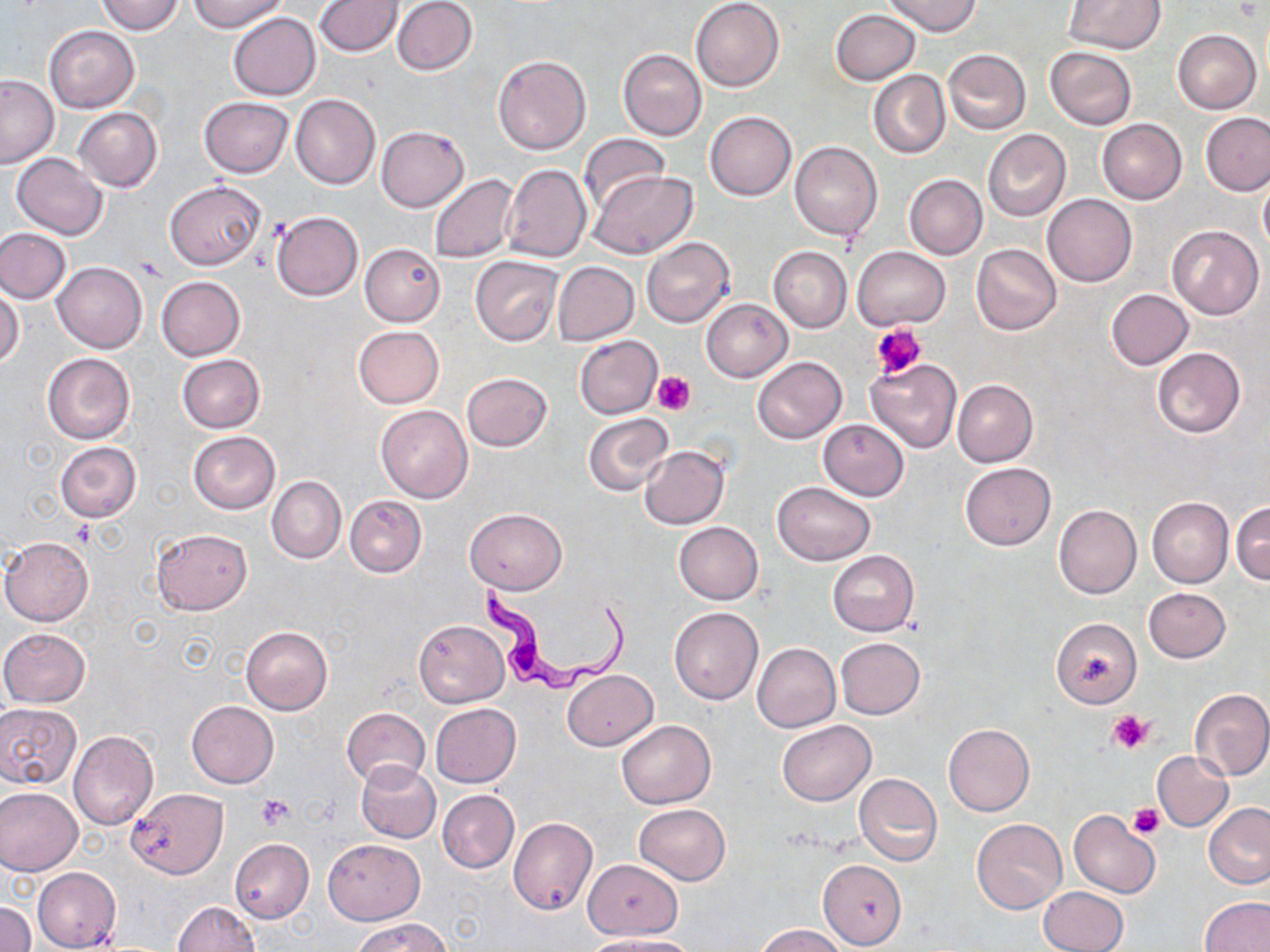

Approximate bounding boxes as named x1/y1/x2/y2 corners in pixels. Platelet locations: (x1=871, y1=322, x2=925, y2=378), (x1=652, y1=370, x2=697, y2=415), (x1=1109, y1=710, x2=1152, y2=754), (x1=256, y1=796, x2=296, y2=830), (x1=1127, y1=803, x2=1165, y2=839). Trypanosoma brucei locations: (x1=477, y1=580, x2=630, y2=695). Uninfected red blood cell locations: (x1=191, y1=0, x2=289, y2=32), (x1=391, y1=0, x2=477, y2=75), (x1=691, y1=0, x2=783, y2=91), (x1=884, y1=0, x2=981, y2=37), (x1=1064, y1=0, x2=1164, y2=52), (x1=97, y1=1, x2=186, y2=35), (x1=316, y1=1, x2=403, y2=56), (x1=831, y1=9, x2=920, y2=85), (x1=227, y1=13, x2=320, y2=100), (x1=44, y1=24, x2=139, y2=113), (x1=1172, y1=29, x2=1261, y2=114), (x1=1188, y1=30, x2=1264, y2=195), (x1=1045, y1=47, x2=1137, y2=130), (x1=618, y1=49, x2=707, y2=140), (x1=943, y1=49, x2=1031, y2=135), (x1=494, y1=55, x2=591, y2=155), (x1=869, y1=69, x2=949, y2=160), (x1=0, y1=75, x2=58, y2=168), (x1=290, y1=94, x2=380, y2=189), (x1=199, y1=96, x2=294, y2=177), (x1=72, y1=107, x2=162, y2=192), (x1=705, y1=111, x2=796, y2=200), (x1=1200, y1=112, x2=1270, y2=195), (x1=1097, y1=118, x2=1186, y2=204), (x1=377, y1=125, x2=468, y2=211), (x1=982, y1=130, x2=1070, y2=221), (x1=578, y1=135, x2=671, y2=213), (x1=789, y1=141, x2=883, y2=241), (x1=12, y1=152, x2=108, y2=239), (x1=501, y1=164, x2=592, y2=263), (x1=1258, y1=170, x2=1270, y2=256), (x1=588, y1=171, x2=697, y2=259), (x1=430, y1=174, x2=518, y2=263), (x1=904, y1=174, x2=987, y2=259), (x1=165, y1=181, x2=266, y2=270), (x1=1042, y1=195, x2=1136, y2=287), (x1=271, y1=211, x2=363, y2=301), (x1=1167, y1=226, x2=1264, y2=319), (x1=0, y1=228, x2=70, y2=303), (x1=641, y1=237, x2=734, y2=327), (x1=359, y1=242, x2=445, y2=327), (x1=972, y1=244, x2=1061, y2=335), (x1=768, y1=246, x2=852, y2=332), (x1=853, y1=246, x2=950, y2=329), (x1=470, y1=256, x2=562, y2=345), (x1=54, y1=262, x2=147, y2=352), (x1=552, y1=262, x2=639, y2=345), (x1=155, y1=276, x2=245, y2=361), (x1=0, y1=287, x2=24, y2=369), (x1=1106, y1=289, x2=1193, y2=369), (x1=702, y1=298, x2=793, y2=382), (x1=353, y1=325, x2=444, y2=408), (x1=574, y1=335, x2=662, y2=419), (x1=1151, y1=347, x2=1246, y2=438), (x1=42, y1=352, x2=135, y2=444), (x1=177, y1=354, x2=265, y2=433), (x1=753, y1=356, x2=846, y2=444), (x1=866, y1=360, x2=961, y2=453), (x1=462, y1=372, x2=551, y2=451), (x1=952, y1=379, x2=1038, y2=467), (x1=376, y1=405, x2=473, y2=503), (x1=584, y1=413, x2=674, y2=495), (x1=818, y1=419, x2=908, y2=500), (x1=187, y1=431, x2=280, y2=514), (x1=55, y1=441, x2=141, y2=523), (x1=640, y1=446, x2=729, y2=530), (x1=959, y1=462, x2=1055, y2=549), (x1=267, y1=476, x2=345, y2=563), (x1=773, y1=482, x2=874, y2=565), (x1=344, y1=495, x2=427, y2=576), (x1=1147, y1=497, x2=1233, y2=587), (x1=1231, y1=501, x2=1269, y2=584), (x1=1054, y1=504, x2=1142, y2=598), (x1=464, y1=508, x2=567, y2=593), (x1=674, y1=522, x2=763, y2=604), (x1=152, y1=528, x2=252, y2=614), (x1=1, y1=537, x2=93, y2=626), (x1=827, y1=551, x2=919, y2=635), (x1=1143, y1=588, x2=1230, y2=662), (x1=670, y1=606, x2=764, y2=704), (x1=1051, y1=618, x2=1142, y2=708), (x1=414, y1=621, x2=508, y2=707), (x1=242, y1=626, x2=333, y2=715), (x1=0, y1=627, x2=91, y2=706), (x1=836, y1=637, x2=924, y2=719), (x1=752, y1=643, x2=841, y2=732), (x1=563, y1=669, x2=658, y2=750), (x1=1190, y1=689, x2=1270, y2=780), (x1=186, y1=701, x2=278, y2=788), (x1=0, y1=702, x2=82, y2=790), (x1=430, y1=703, x2=521, y2=787), (x1=341, y1=706, x2=430, y2=786), (x1=616, y1=719, x2=717, y2=809), (x1=777, y1=720, x2=875, y2=806), (x1=943, y1=724, x2=1034, y2=816), (x1=69, y1=730, x2=158, y2=829), (x1=1152, y1=751, x2=1232, y2=831), (x1=356, y1=761, x2=440, y2=842), (x1=853, y1=773, x2=942, y2=866), (x1=0, y1=786, x2=83, y2=875), (x1=129, y1=788, x2=228, y2=878), (x1=438, y1=790, x2=518, y2=873), (x1=633, y1=803, x2=730, y2=885), (x1=1203, y1=803, x2=1270, y2=889), (x1=1069, y1=810, x2=1160, y2=898), (x1=508, y1=817, x2=597, y2=916), (x1=972, y1=819, x2=1066, y2=913), (x1=230, y1=839, x2=314, y2=923), (x1=323, y1=839, x2=424, y2=924), (x1=582, y1=859, x2=682, y2=939), (x1=817, y1=859, x2=906, y2=951), (x1=32, y1=867, x2=121, y2=951), (x1=1038, y1=886, x2=1127, y2=952), (x1=1201, y1=897, x2=1269, y2=952), (x1=0, y1=901, x2=35, y2=952), (x1=173, y1=902, x2=260, y2=952), (x1=352, y1=917, x2=453, y2=952), (x1=756, y1=924, x2=847, y2=952), (x1=585, y1=934, x2=699, y2=952). Slide-level diagnosis: Trypanosoma brucei. Optical microscopy. May-Grünwald-Giemsa stain. Thin blood smear. 1000x magnification. Single field of view. Image is 1270×952 pixels.